Name the parasite shown.
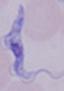

This is a trypanosome.

Summary:
  - Magnification: 1000x
  - Modality: photomicrograph